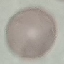

result: negative for malaria parasites
stain: Giemsa
preparation: thin smear
capture: smartphone camera at the microscope eyepiece
image_type: cell patch, automatically extracted from a larger field of view and resized to 64 × 64 pixels